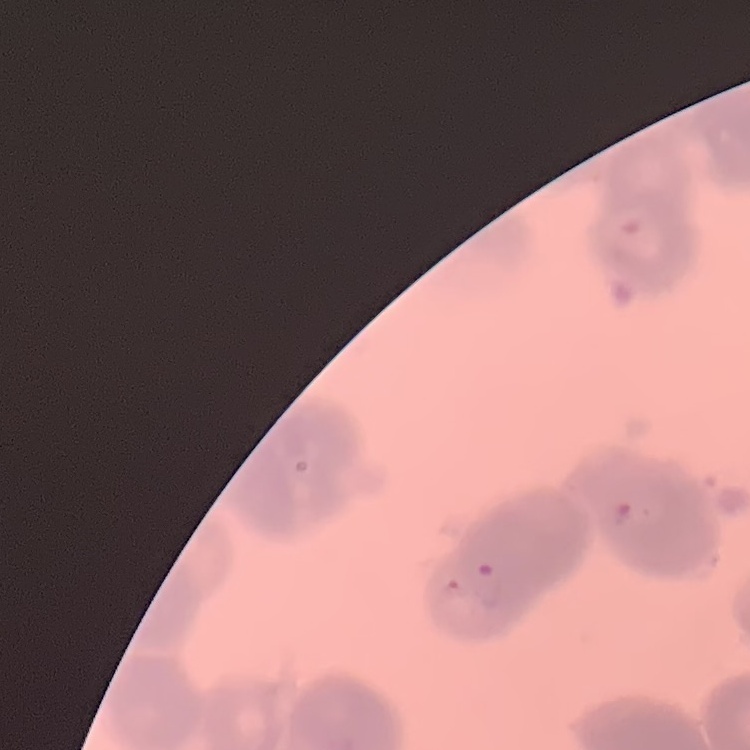
The red blood cells show rouleaux formation. Stained with either Field's or Giemsa. Thin blood film. Square crop of a larger photomicrograph.